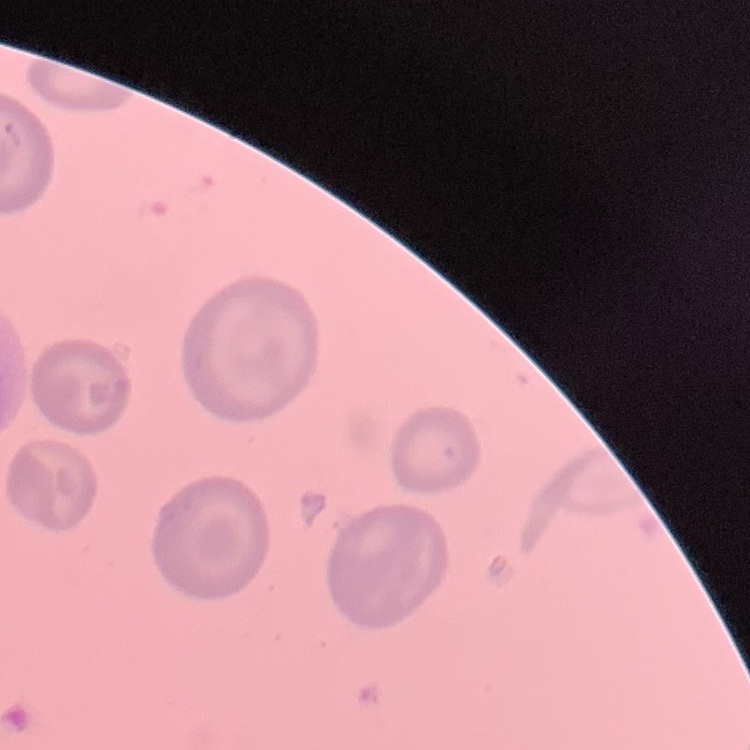

Summary:
  - Erythrocyte morphology: no rouleaux formation
  - Preparation: thin blood film
  - Image type: one tile cut from a larger photomicrograph
  - Stain: Field's or Giemsa